Give the position of every malaria parasite.
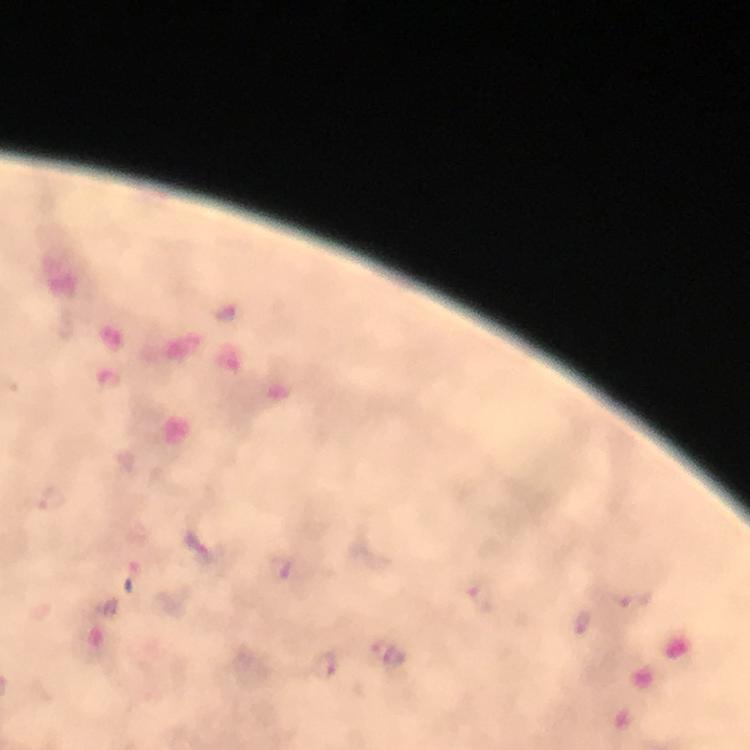
Approximate object centers, in pixels from the top-left corner.
Malaria parasites: (x=196, y=544), (x=280, y=567), (x=388, y=654), (x=323, y=666).

{
  "image_size": "750×750 pixels",
  "preparation": "thick smear",
  "capture": "smartphone camera through the microscope",
  "stain": "Giemsa",
  "cropped_from": "a single field of view",
  "context": "from a diagnostic examination for malaria",
  "magnification": "100x",
  "immersion_oil": "applied"
}